Assess the morphology of the red blood cells.
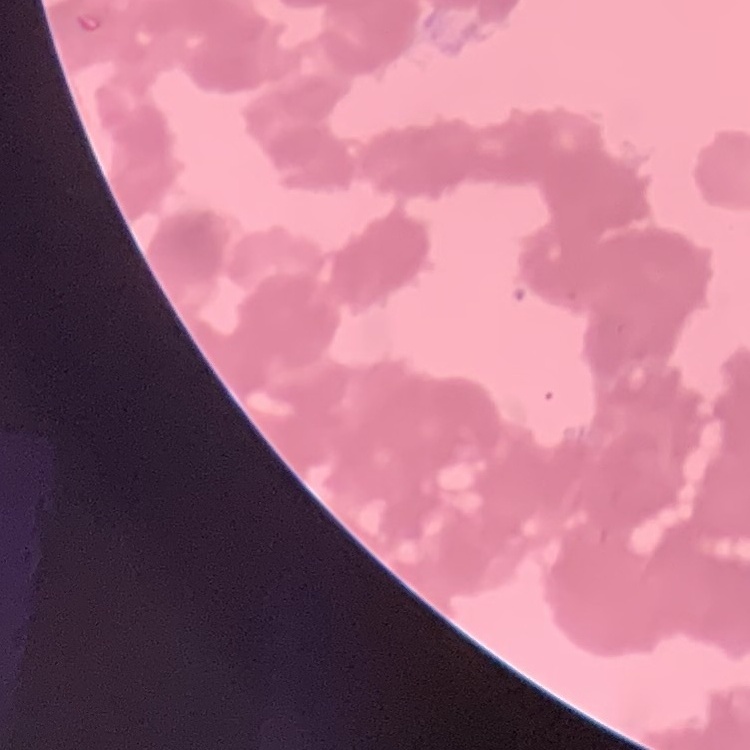

They show rouleaux formation.

preparation: thin peripheral smear
stain: Field's or Giemsa
image_type: one tile cut from a larger photomicrograph